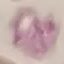

Summary:
  - Result: negative for malaria parasites
  - Capture: smartphone through the microscope eyepiece
  - Image type: automatically extracted cell patch, resized to 64 × 64 pixels
  - Stain: Giemsa
  - Preparation: thin blood film